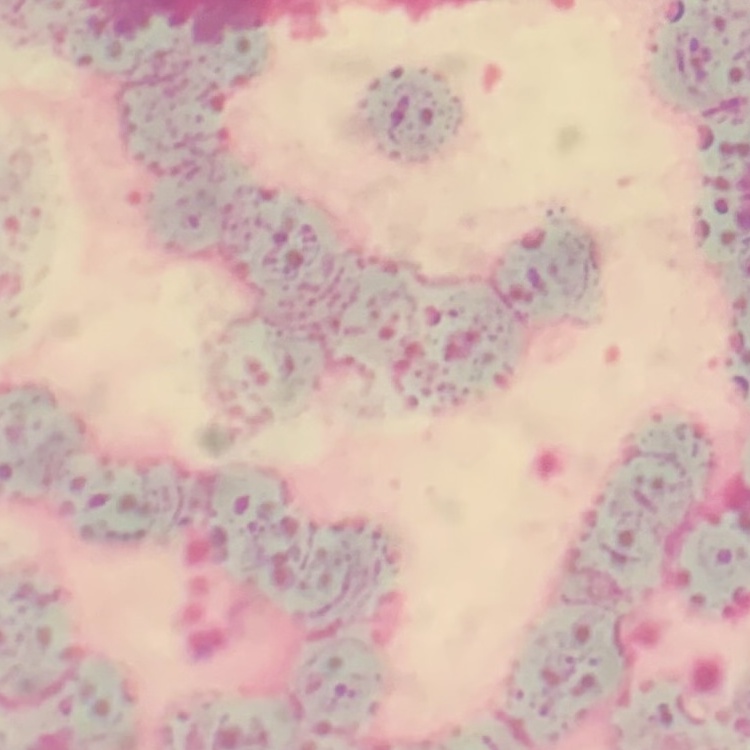
The erythrocytes exhibit rouleaux formation. Thin blood smear. Square crop of a larger photomicrograph. Field's or Giemsa stain.